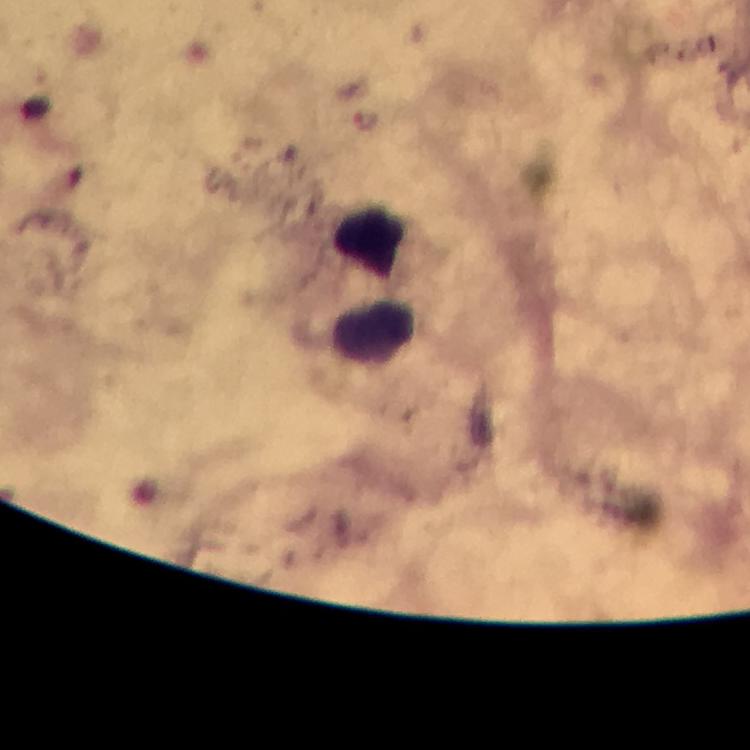

Approximate centers as (x, y) in pixels. Malaria parasite locations: (366, 120). Leukocyte locations: (368, 242), (374, 329). Cropped region of a single field of view. Image is 750×750 pixels. Immersion oil applied. Thick blood film. From a malaria diagnostic workup. Photographed through the microscope with a smartphone camera. Giemsa-stained preparation. 100x magnification.